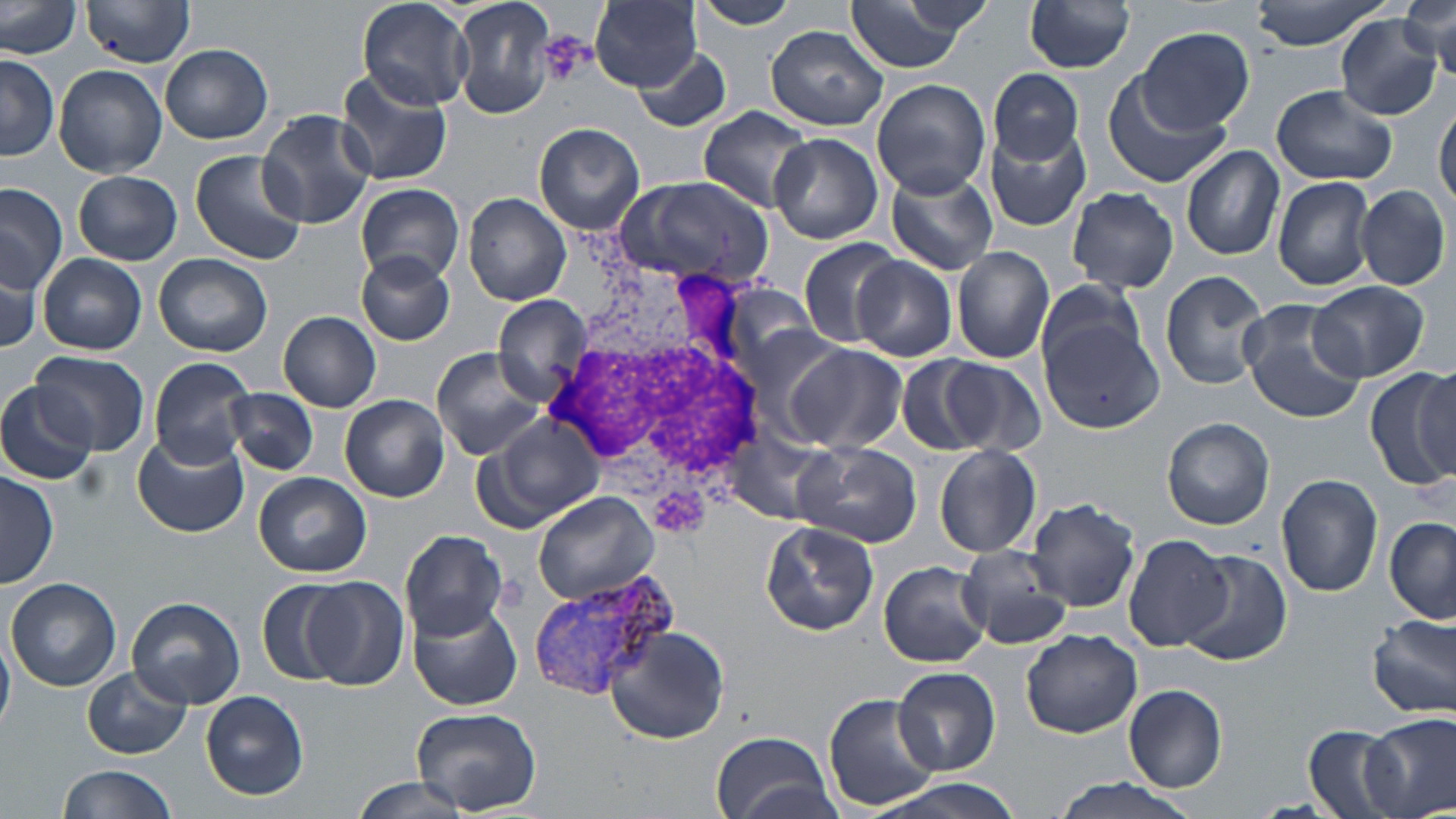
Summary:
  - Coordinate format: approximate bounding boxes as [x1, y1, x2, y2] in pixels
  - White blood cell locations: [547, 263, 763, 538]
  - Uninfected red blood cell locations: [357, 0, 472, 111], [451, 0, 557, 119], [691, 0, 801, 30], [842, 0, 976, 73], [1025, 0, 1136, 73], [1249, 0, 1392, 49], [80, 1, 195, 67], [591, 1, 703, 91], [84, 2, 195, 68], [1013, 2, 1121, 145], [0, 3, 82, 58], [1402, 4, 1455, 76], [1336, 16, 1443, 120], [766, 25, 890, 130], [1136, 27, 1254, 135], [160, 43, 273, 145], [633, 46, 733, 134], [1, 54, 59, 162], [54, 64, 167, 178], [989, 69, 1085, 164], [336, 71, 453, 187], [1102, 76, 1230, 187], [872, 78, 991, 198], [1272, 86, 1395, 185], [1434, 105, 1455, 211], [697, 106, 815, 211], [257, 109, 375, 229], [534, 122, 646, 235], [985, 127, 1092, 231], [770, 134, 883, 244], [1181, 145, 1285, 260], [189, 150, 304, 264], [884, 169, 998, 276], [73, 170, 182, 265], [1273, 175, 1375, 291], [612, 177, 773, 289], [355, 183, 466, 286], [0, 185, 65, 291], [1357, 185, 1449, 291], [1067, 186, 1179, 293], [463, 193, 571, 307], [798, 236, 902, 349], [952, 246, 1054, 363], [154, 253, 273, 356], [356, 253, 456, 347], [39, 254, 146, 354], [854, 255, 956, 360], [0, 258, 46, 358], [1160, 270, 1270, 390], [1035, 279, 1148, 380], [1309, 281, 1429, 382], [492, 295, 594, 395], [1239, 303, 1366, 423], [1038, 309, 1163, 433], [279, 312, 382, 412], [783, 343, 906, 454], [431, 347, 552, 462], [30, 351, 147, 455], [897, 355, 992, 454], [149, 357, 256, 468], [938, 358, 1048, 457], [1369, 365, 1456, 490], [1408, 368, 1454, 481], [0, 380, 104, 487], [226, 388, 318, 475], [341, 394, 448, 501], [484, 412, 604, 527], [1163, 417, 1276, 531], [131, 434, 248, 537], [792, 439, 921, 548], [933, 445, 1042, 559], [1, 472, 58, 589], [255, 472, 371, 577], [1277, 473, 1383, 597], [532, 492, 659, 604], [1025, 497, 1140, 611], [1385, 515, 1456, 622], [761, 522, 879, 636], [400, 529, 509, 638], [1124, 535, 1235, 652], [956, 545, 1073, 650], [1176, 547, 1293, 667], [879, 561, 991, 667], [7, 577, 120, 690], [302, 577, 410, 690], [260, 579, 352, 688], [127, 596, 245, 709], [407, 601, 521, 710], [1367, 613, 1456, 721], [601, 625, 732, 747], [1021, 629, 1144, 739], [0, 636, 15, 735], [84, 666, 190, 759], [892, 667, 1001, 775], [1123, 683, 1228, 793], [200, 690, 309, 801], [825, 693, 943, 812], [412, 707, 541, 816], [1366, 713, 1456, 819], [1301, 725, 1405, 819], [711, 731, 833, 819], [58, 764, 181, 819], [350, 776, 478, 819], [1045, 778, 1206, 819], [874, 779, 1027, 819]
  - Plasmodium vivax-infected red blood cell locations: [529, 569, 678, 701]
  - Platelet locations: [536, 31, 595, 86]
  - Slide-level diagnosis: Plasmodium vivax
  - Modality: light microscopy
  - Preparation: thin blood smear
  - Magnification: 1000x
  - Image size: 1456×819 pixels
  - Field of view: single
  - Stain: May-Grünwald-Giemsa